Locate every Plasmodium parasite.
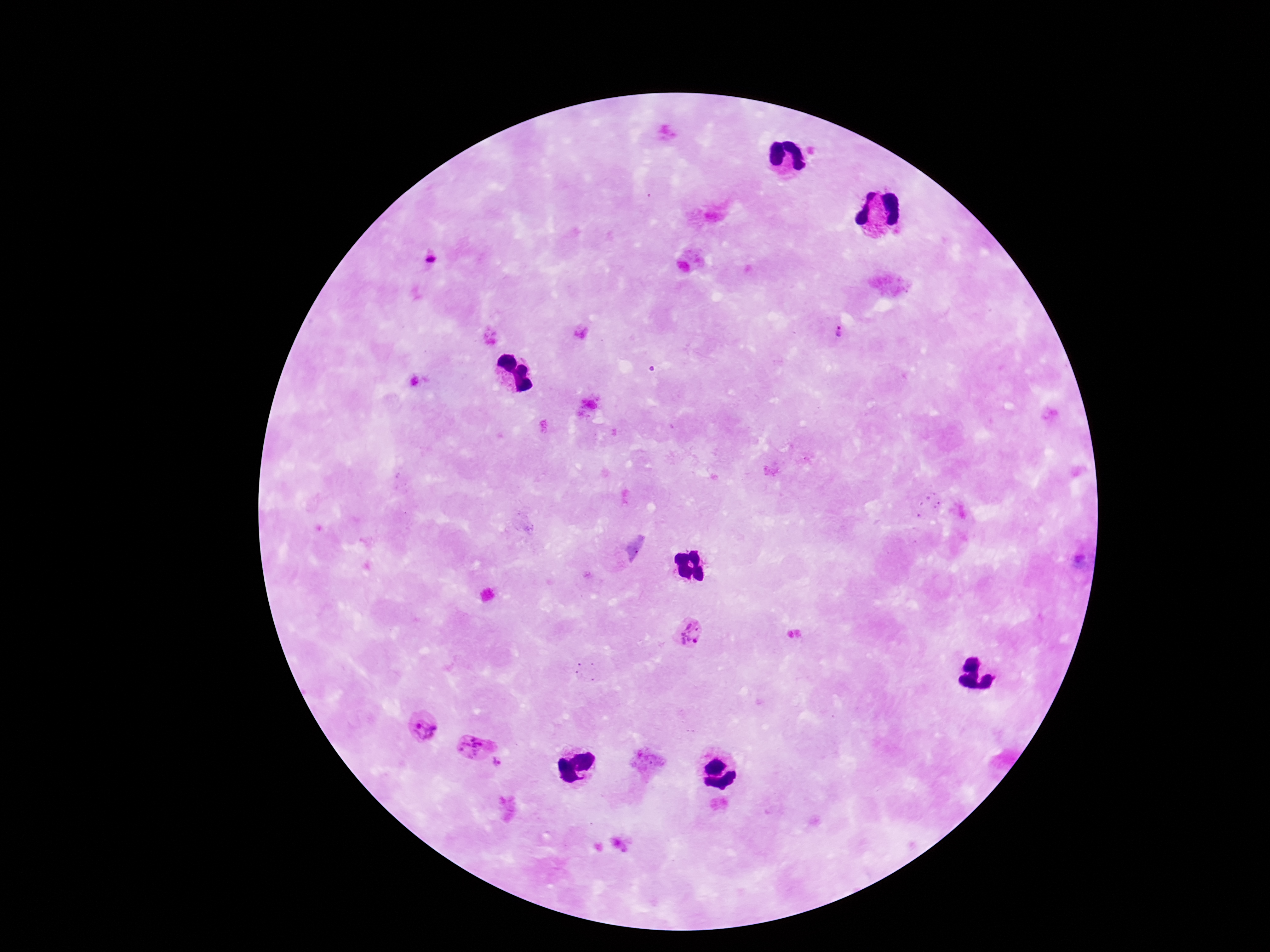

Approximate centers as (x, y) in pixels.
Plasmodium parasites: (429, 258), (841, 327), (688, 632), (425, 727), (476, 737), (500, 766).

Giemsa-stained preparation. Patient malaria status: infected. 100x magnification. Image is 1270×952 pixels. Single field of view. Thick peripheral-blood smear. Photographed through the microscope eyepiece with a smartphone camera.